Report the malaria status of this cell.
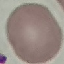
Uninfected.

{
  "stain": "Giemsa",
  "capture": "smartphone through the microscope eyepiece",
  "image_type": "automatically extracted cell patch, resized to 64 × 64 pixels",
  "preparation": "thin blood smear"
}